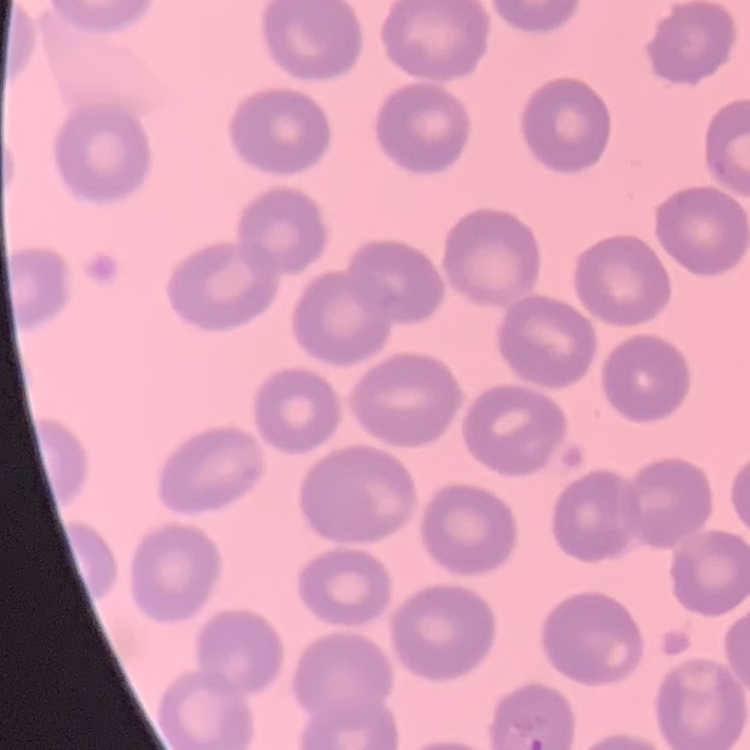
Summary:
  - Erythrocyte morphology: no rouleaux formation
  - Preparation: thin blood film
  - Stain: Field's or Giemsa
  - Image type: one tile cut from a larger photomicrograph